Classify the preparation.
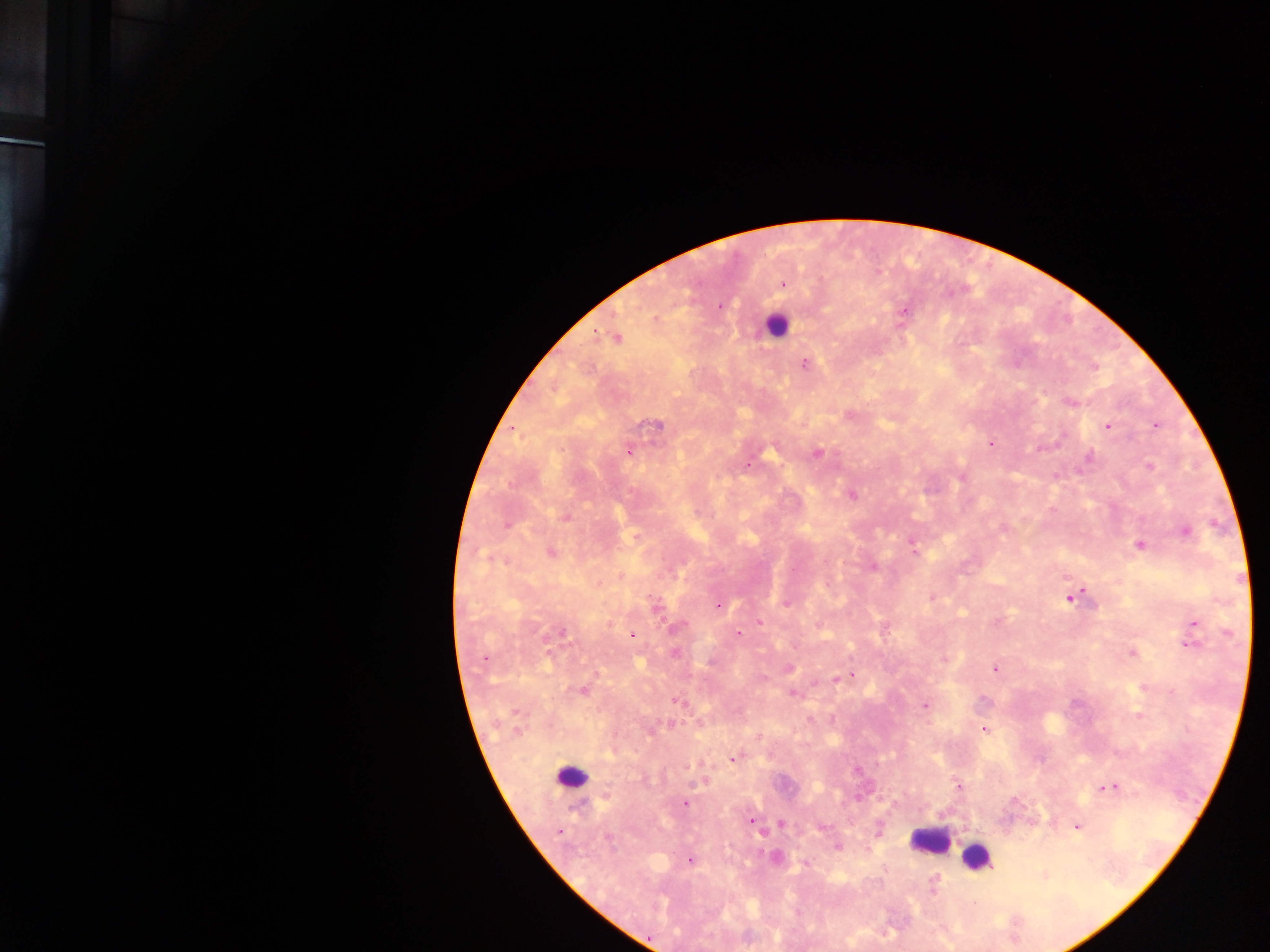
This is a thick smear.

country = Ghana
image size = 1270×952 pixels
capture = mobile-phone photograph through a microscope
malaria parasite locations = approximate centers as x y in pixels: 783 285; 720 306; 904 310; 616 338; 805 364; 1070 402; 656 424; 1155 425; 1107 426; 990 444; 628 451; 817 453; 1090 458; 748 466; 1150 467; 852 494; 566 516; 507 525; 1002 530; 1186 532; 1139 546; 551 553; 915 553; 488 557; 873 567; 792 569; 932 597; 1071 597; 786 604; 718 605; 656 610; 759 622; 1195 624; 679 626; 562 633; 738 633; 633 635; 1190 645; 674 653; 1132 653; 485 659; 944 659; 789 668; 995 669; 851 675; 836 679; 583 690; 792 693; 677 702; 924 706; 517 713; 1139 715; 983 729; 517 731; 652 731; 733 759; 700 783; 958 786; 1110 786; 685 803; 751 821; 782 824; 1077 826; 559 832; 609 840; 838 847; 690 860; 806 864; 933 886; 975 904
leukocyte locations = approximate centers as x y in pixels: 775 326; 571 777; 929 840; 976 856
field of view = single